State the blood parasite species.
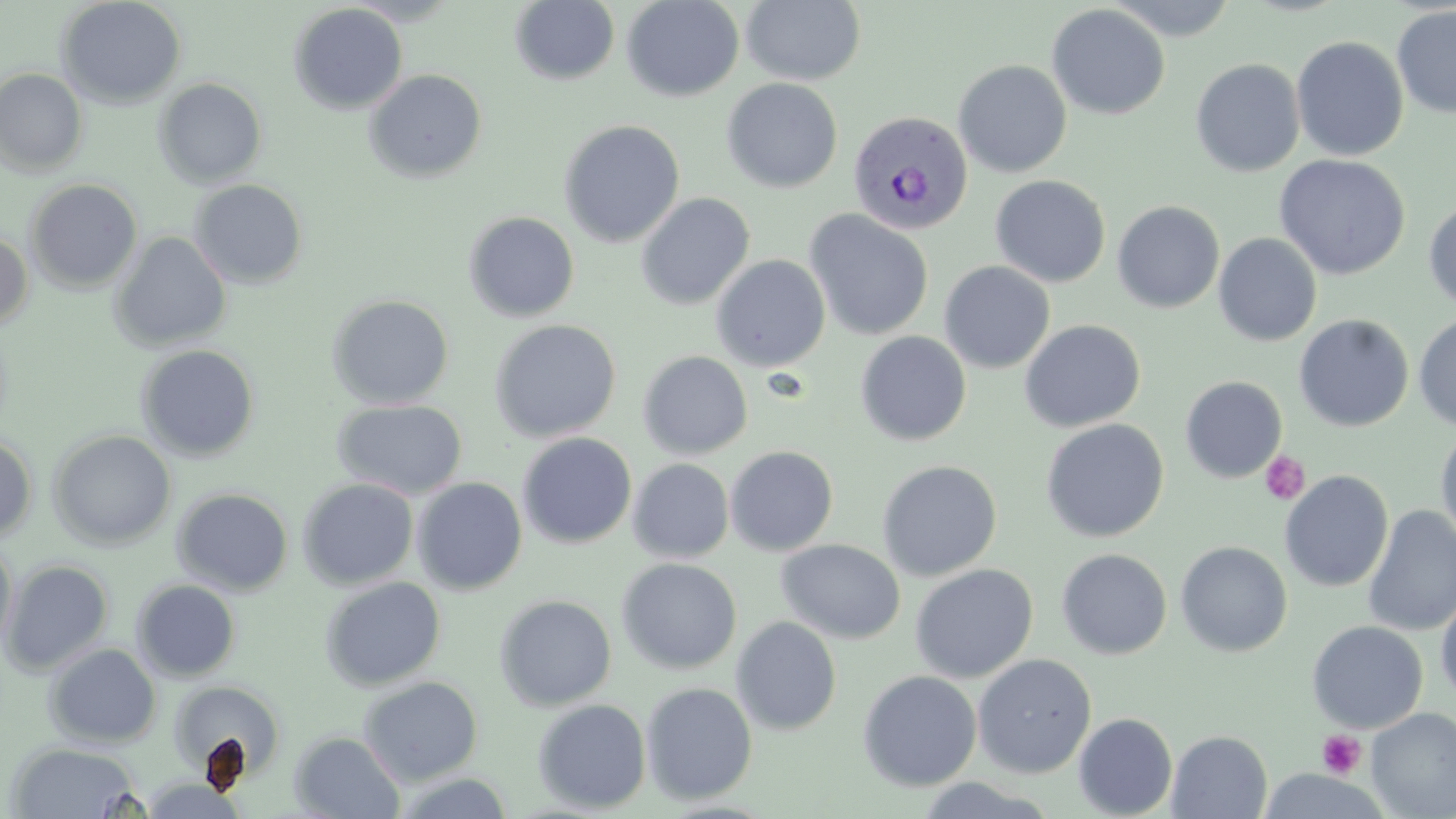

Plasmodium vivax.

{
  "platelet_locations": "approximate bounding boxes as (x1, y1, x2, y2) in pixels: (1259, 451, 1310, 505), (1317, 730, 1367, 779)",
  "modality": "light microscopy",
  "magnification": "1000x",
  "image_size": "1456×819 pixels",
  "stain": "May-Grünwald-Giemsa",
  "field_of_view": "single",
  "uninfected_red_blood_cell_locations": "approximate bounding boxes as (x1, y1, x2, y2) in pixels: (55, 0, 187, 110), (621, 0, 745, 102), (741, 0, 866, 86), (1104, 0, 1239, 41), (510, 1, 620, 85), (288, 3, 408, 115), (1047, 4, 1170, 119), (1392, 5, 1456, 119), (1291, 36, 1409, 161), (1190, 59, 1305, 177), (953, 60, 1072, 178), (0, 67, 88, 177), (364, 69, 487, 183), (154, 78, 267, 188), (721, 78, 843, 193), (558, 119, 685, 248), (1274, 153, 1411, 280), (990, 175, 1111, 288), (26, 179, 143, 294), (189, 179, 308, 290), (636, 192, 755, 310), (1423, 198, 1456, 311), (1113, 201, 1225, 313), (804, 209, 934, 341), (463, 211, 580, 322), (0, 230, 33, 331), (109, 231, 232, 353), (1213, 233, 1322, 346), (711, 254, 831, 372), (939, 260, 1056, 374), (326, 294, 454, 410), (1414, 311, 1456, 432), (1294, 314, 1414, 432), (489, 319, 621, 443), (1019, 319, 1146, 433), (855, 331, 972, 446), (135, 344, 260, 462), (638, 351, 753, 459), (1180, 376, 1287, 483), (332, 398, 467, 500), (1040, 418, 1169, 542), (1435, 424, 1456, 552), (48, 429, 176, 551), (0, 433, 37, 542), (517, 433, 637, 548), (725, 445, 838, 556), (628, 458, 734, 563), (877, 460, 1002, 581), (1279, 470, 1394, 592), (298, 477, 419, 590), (412, 477, 528, 594), (171, 487, 294, 596), (1362, 505, 1456, 637), (0, 539, 17, 656), (777, 539, 905, 644), (1175, 540, 1293, 657), (1056, 548, 1172, 659), (616, 558, 742, 675), (2, 560, 114, 676), (910, 563, 1038, 683), (320, 577, 445, 692), (132, 579, 241, 682), (1435, 586, 1456, 706), (494, 594, 617, 711), (731, 616, 842, 735), (1306, 620, 1428, 733), (44, 643, 161, 748), (973, 653, 1097, 778), (857, 670, 982, 791), (358, 675, 483, 786), (167, 679, 287, 784), (641, 682, 757, 804), (533, 698, 651, 813), (1366, 707, 1456, 818), (1073, 713, 1178, 818), (1167, 730, 1273, 819), (290, 731, 405, 818), (5, 741, 144, 818), (388, 770, 516, 818), (910, 777, 1059, 818), (135, 778, 251, 818)",
  "plasmodium_vivax_infected_red_blood_cell_locations": "approximate bounding boxes as (x1, y1, x2, y2) in pixels: (848, 111, 973, 235)",
  "preparation": "thin blood smear"
}